Assess this cell for malaria.
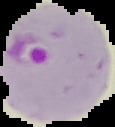

Parasitized.

Summary:
  - Preparation: thin blood film
  - Image type: segmented cell region on a black background
  - Image size: 115×127 pixels